Report the malaria status of this cell.
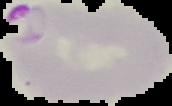
It is parasitized.

image_type: segmented cell region on a black background
image_size: 172×106 pixels
preparation: thin blood film